Assess for Plasmodium parasites.
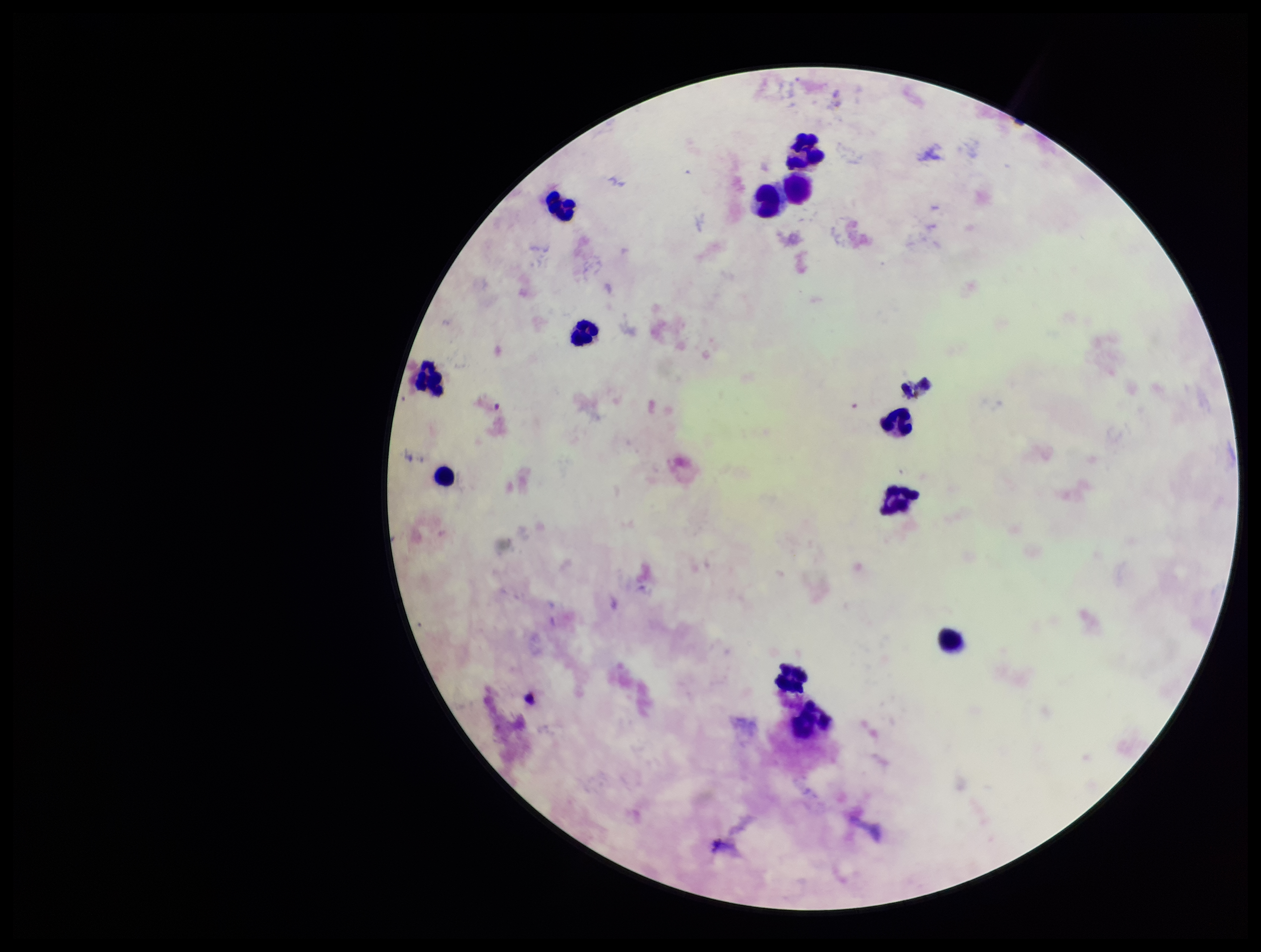

None seen.

Summary:
  - Stain: Giemsa
  - Capture: smartphone photograph through the microscope eyepiece
  - Image size: 1261×952 pixels
  - Leukocyte count: 12
  - Patient malaria status: negative
  - Field of view: single
  - Preparation: thick smear
  - Parasite count: 0